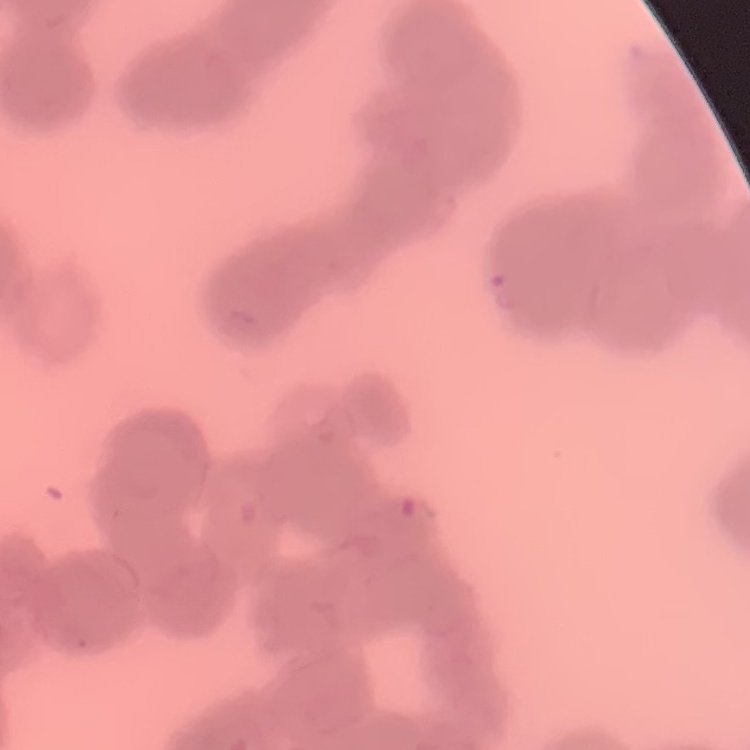
erythrocyte morphology = rouleaux formation
preparation = thin blood smear
image type = one tile cut from a larger photomicrograph
stain = Field's or Giemsa